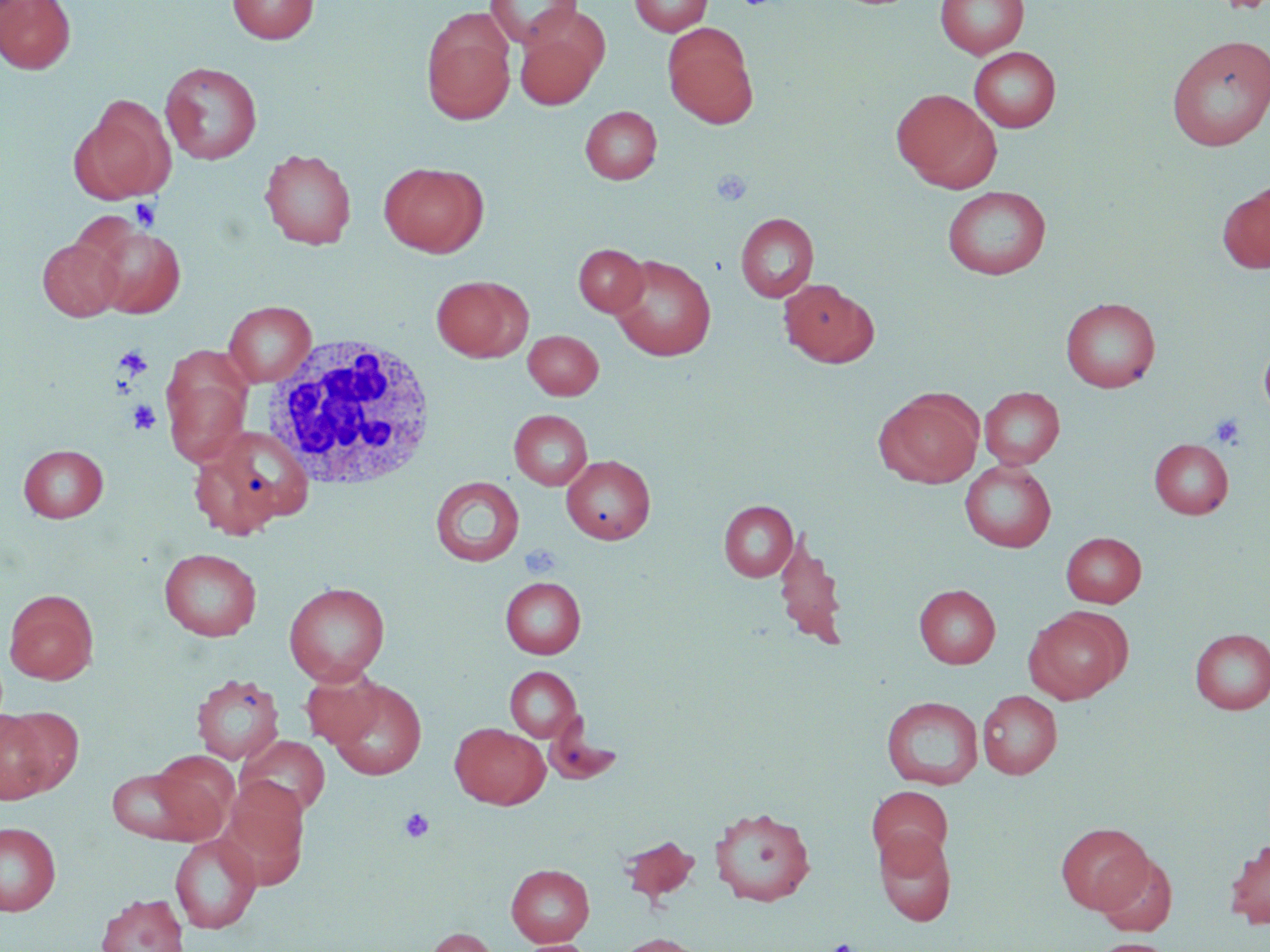
Approximate bounding boxes as [x1, y1, x2, y2] in pixels. Platelet locations: [712, 169, 752, 206], [130, 199, 161, 231], [115, 346, 152, 378], [128, 400, 161, 435], [1209, 413, 1245, 450], [520, 544, 561, 578], [400, 807, 434, 843], [826, 939, 859, 952]. White blood cell locations: [262, 335, 440, 491]. Uninfected red blood cell locations: [0, 0, 76, 74], [228, 0, 319, 44], [484, 0, 583, 49], [629, 0, 713, 36], [936, 0, 1028, 59], [421, 15, 515, 123], [514, 22, 605, 109], [662, 23, 759, 128], [1165, 35, 1270, 151], [969, 47, 1061, 133], [160, 61, 263, 164], [892, 88, 1001, 192], [70, 95, 175, 204], [580, 105, 662, 184], [259, 148, 357, 249], [379, 162, 488, 258], [1217, 181, 1270, 275], [942, 186, 1051, 280], [736, 213, 819, 302], [87, 224, 186, 318], [37, 238, 124, 321], [574, 244, 648, 317], [609, 254, 716, 361], [431, 275, 531, 362], [779, 279, 879, 368], [1060, 297, 1160, 392], [223, 301, 316, 387], [523, 330, 603, 400], [1258, 332, 1270, 424], [162, 361, 251, 468], [980, 387, 1064, 468], [875, 389, 983, 488], [509, 409, 593, 490], [188, 430, 306, 539], [1149, 438, 1234, 519], [18, 444, 109, 522], [561, 455, 656, 544], [960, 459, 1056, 552], [431, 476, 524, 566], [719, 501, 798, 581], [773, 529, 849, 649], [1061, 532, 1146, 607], [159, 548, 261, 641], [500, 576, 586, 658], [283, 582, 390, 684], [914, 584, 1000, 668], [3, 589, 99, 684], [1024, 608, 1129, 703], [1189, 628, 1270, 715], [505, 666, 581, 742], [300, 667, 386, 748], [191, 673, 285, 765], [328, 679, 427, 780], [977, 690, 1062, 779], [882, 696, 983, 790], [0, 707, 69, 803], [450, 722, 549, 809], [237, 735, 330, 819], [147, 750, 239, 842], [106, 764, 210, 845], [219, 778, 309, 889], [868, 785, 953, 869], [708, 805, 816, 906], [0, 822, 61, 915], [1055, 822, 1152, 913], [874, 829, 956, 925], [169, 833, 261, 934], [619, 835, 700, 905], [1224, 839, 1270, 929], [1094, 852, 1177, 937], [506, 863, 594, 946], [97, 892, 189, 952], [422, 926, 499, 952], [613, 933, 709, 952], [1088, 938, 1175, 952], [519, 939, 596, 952]. Slide-level diagnosis: negative for blood parasites. Thin blood film. Image is 1270×952 pixels. One field of a larger specimen. Light microscopy. May-Grünwald-Giemsa stain. Captured at 1000x magnification.